Locate and identify every blood parasite.
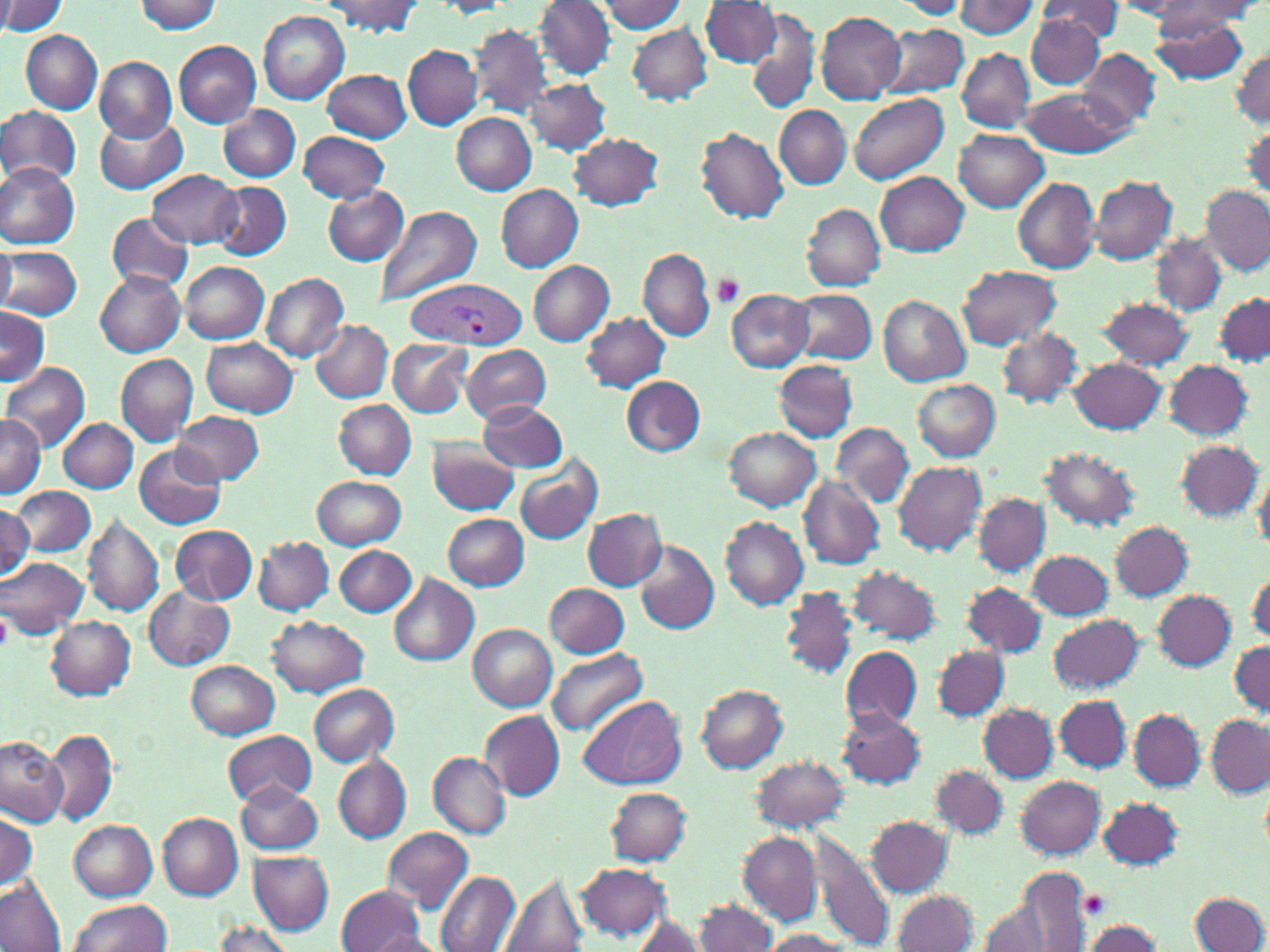
Approximate bounding boxes as (x1,y1)-(x2,y2) corner pairs in pixels.
Plasmodium vivax-infected red blood cells: (402,277)-(527,349).
No Plasmodium falciparum, Plasmodium ovale, Plasmodium malariae, Babesia divergens, or Trypanosoma brucei observed.

Summary:
  - Uninfected red blood cell locations: (0,0)-(66,36), (326,0)-(421,34), (534,0)-(616,80), (895,0)-(967,20), (952,0)-(1041,39), (133,1)-(222,33), (431,1)-(514,18), (597,1)-(687,33), (1113,1)-(1196,19), (1161,1)-(1261,26), (701,2)-(781,67), (1035,2)-(1125,40), (1152,4)-(1251,45), (259,10)-(350,104), (815,11)-(907,105), (1150,11)-(1249,84), (746,12)-(820,114), (1027,14)-(1104,89), (627,22)-(713,104), (879,24)-(970,98), (471,25)-(552,118), (20,30)-(102,112), (173,41)-(260,127), (403,44)-(482,130), (957,48)-(1034,132), (1080,49)-(1161,131), (1232,49)-(1269,127), (95,57)-(176,141), (325,70)-(413,142), (525,78)-(609,154), (1020,87)-(1129,156), (849,92)-(948,185), (0,105)-(82,187), (219,105)-(301,180), (775,105)-(850,189), (452,113)-(537,194), (94,118)-(188,194), (1243,123)-(1270,202), (695,126)-(789,225), (954,129)-(1049,212), (298,130)-(390,203), (567,133)-(664,211), (0,162)-(79,250), (150,169)-(241,248), (876,172)-(969,255), (1089,176)-(1178,266), (1012,177)-(1101,274), (213,181)-(291,260), (496,182)-(583,270), (323,186)-(408,266), (1202,187)-(1268,274), (801,203)-(886,291), (377,205)-(481,308), (105,215)-(193,291), (1151,235)-(1225,315), (0,243)-(14,314), (0,245)-(83,320), (638,247)-(716,340), (529,260)-(614,346), (180,261)-(269,344), (959,265)-(1060,350), (94,268)-(185,357), (261,273)-(350,363), (725,288)-(815,370), (789,288)-(876,364), (1214,292)-(1269,369), (878,296)-(970,386), (1098,297)-(1195,370), (1,305)-(48,386), (581,312)-(670,392), (311,319)-(393,402), (995,327)-(1083,409), (203,338)-(298,416), (387,339)-(472,418), (461,344)-(553,423), (116,354)-(198,446), (1070,357)-(1167,434), (773,359)-(857,443), (0,360)-(90,452), (1164,361)-(1254,441), (622,376)-(704,456), (912,378)-(1001,461), (323,399)-(410,550), (334,400)-(415,478), (476,401)-(568,472), (176,412)-(263,486), (0,415)-(46,496), (60,418)-(137,492), (833,422)-(913,504), (725,427)-(820,510), (428,438)-(520,515), (1176,439)-(1262,522), (135,444)-(225,530), (1039,445)-(1139,531), (514,453)-(603,545), (893,460)-(988,556), (1253,469)-(1270,555), (311,476)-(406,549), (799,478)-(884,570), (11,484)-(96,557), (974,493)-(1049,575), (0,504)-(35,584), (583,507)-(667,591), (83,513)-(164,616), (443,513)-(529,590), (720,516)-(810,610), (1109,520)-(1194,601), (171,525)-(257,604), (254,535)-(334,614), (246,539)-(417,618), (634,540)-(719,634), (334,544)-(418,617), (1028,549)-(1113,620), (0,557)-(88,637), (846,565)-(943,645), (1247,569)-(1269,648), (387,573)-(478,667), (545,582)-(629,657), (963,582)-(1045,657), (144,587)-(233,669), (780,587)-(857,681), (1153,590)-(1235,670), (1049,613)-(1142,692), (267,615)-(369,698), (46,616)-(135,699), (468,624)-(557,710), (1229,641)-(1270,717), (840,644)-(923,730), (933,645)-(1009,721), (545,646)-(646,735), (186,659)-(278,738), (308,683)-(399,766), (695,684)-(789,774), (576,694)-(686,789), (1056,695)-(1130,771), (978,703)-(1057,781), (837,708)-(923,787), (1129,709)-(1205,789), (479,710)-(564,800), (1205,716)-(1269,795), (46,729)-(119,826), (222,731)-(317,807), (0,736)-(68,825), (428,752)-(511,840), (333,753)-(411,844), (750,755)-(850,832), (931,764)-(1007,838), (1015,776)-(1107,857), (236,782)-(323,854), (605,786)-(691,865), (1099,796)-(1182,869), (0,812)-(39,892), (158,812)-(243,898), (867,817)-(953,897), (69,819)-(158,900), (382,827)-(474,911), (810,829)-(895,952), (737,832)-(821,925), (248,850)-(332,934), (576,863)-(671,940), (436,870)-(520,952), (987,872)-(1092,950), (496,873)-(589,952), (0,874)-(67,952), (337,885)-(425,951), (893,890)-(978,951), (1190,892)-(1270,952), (69,898)-(171,952), (694,898)-(778,951), (973,898)-(1060,952), (629,913)-(709,951), (1081,919)-(1162,951), (211,922)-(300,952), (759,929)-(853,951), (366,930)-(444,951)
  - Platelet locations: (711,273)-(743,308), (1080,891)-(1109,919)
  - Slide-level diagnosis: Plasmodium vivax
  - Image size: 1270×952 pixels
  - Field of view: single
  - Preparation: thin blood film
  - Stain: May-Grünwald-Giemsa
  - Magnification: 1000x
  - Modality: light microscopy